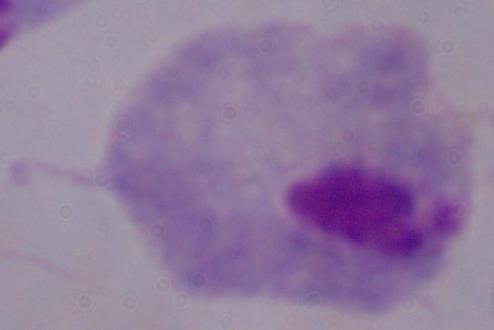
{
  "identification": "trichomonad",
  "magnification": "1000x",
  "modality": "micrograph"
}